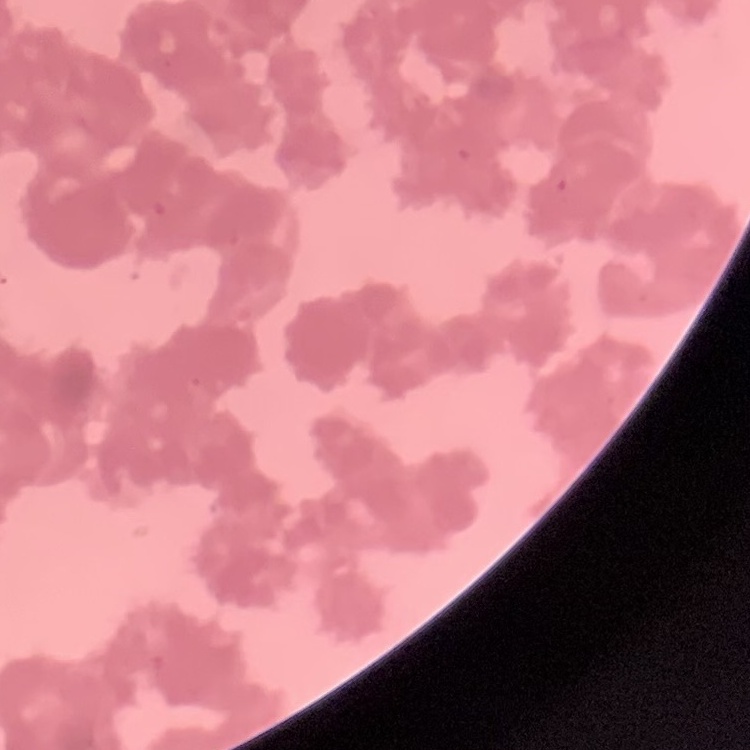

The red blood cells exhibit rouleaux formation. Square crop of a larger photomicrograph. Thin blood smear. Stained with either Field's or Giemsa.